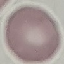

Summary:
  - Malaria status: uninfected
  - Preparation: thin smear
  - Image type: cell patch, automatically extracted from a larger field of view and resized to 64 × 64 pixels
  - Capture: smartphone through the microscope eyepiece
  - Stain: Giemsa